Locate and identify every blood parasite.
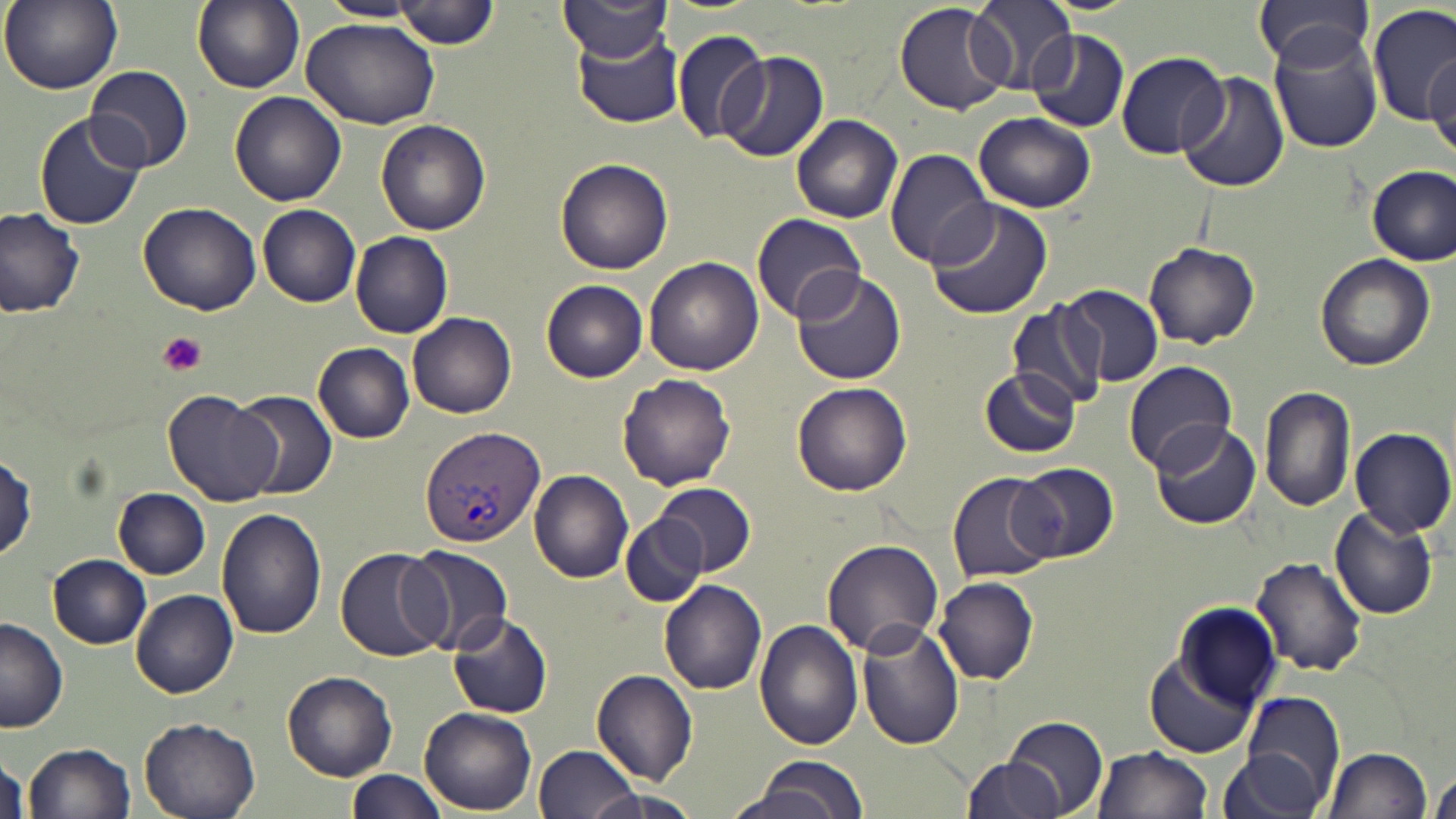
Approximate bounding boxes as [x1, y1, x2, y2] in pixels.
Plasmodium vivax-infected red blood cells: [420, 427, 545, 548].
No Plasmodium falciparum, Plasmodium ovale, Plasmodium malariae, Babesia divergens, or Trypanosoma brucei observed.

Platelet locations: [156, 331, 209, 376]. Uninfected red blood cell locations: [1, 0, 123, 94], [192, 0, 304, 92], [318, 0, 425, 23], [397, 0, 499, 49], [970, 0, 1079, 92], [1254, 0, 1375, 72], [555, 1, 672, 64], [895, 2, 1012, 115], [1369, 5, 1455, 127], [299, 13, 441, 131], [670, 28, 771, 144], [1028, 28, 1129, 133], [572, 29, 685, 128], [1269, 33, 1383, 154], [1029, 37, 1227, 140], [718, 51, 828, 163], [1116, 51, 1230, 160], [1426, 54, 1456, 158], [86, 65, 193, 175], [1175, 70, 1291, 192], [229, 92, 346, 207], [971, 109, 1096, 214], [34, 112, 146, 231], [791, 113, 902, 223], [375, 120, 491, 236], [885, 149, 995, 267], [555, 157, 673, 276], [1368, 166, 1454, 265], [925, 199, 1054, 320], [138, 201, 262, 315], [257, 205, 361, 307], [0, 207, 84, 317], [751, 213, 866, 322], [351, 232, 453, 338], [1142, 242, 1260, 348], [1315, 254, 1434, 370], [643, 256, 762, 375], [789, 269, 906, 385], [540, 280, 648, 382], [1060, 286, 1163, 386], [1008, 301, 1108, 409], [408, 312, 517, 418], [314, 342, 414, 444], [1122, 361, 1238, 476], [978, 367, 1081, 457], [617, 374, 737, 489], [792, 382, 911, 497], [1259, 385, 1357, 514], [233, 388, 337, 500], [161, 389, 282, 506], [1149, 420, 1263, 531], [1350, 427, 1455, 540], [1, 450, 37, 561], [1012, 462, 1119, 563], [529, 469, 634, 582], [948, 470, 1064, 584], [651, 481, 755, 575], [113, 487, 210, 578], [1328, 507, 1440, 620], [216, 509, 327, 640], [621, 514, 705, 606], [822, 539, 944, 655], [400, 543, 514, 654], [335, 545, 449, 662], [48, 554, 152, 648], [1250, 555, 1368, 679], [935, 576, 1040, 686], [659, 580, 769, 694], [132, 589, 240, 696], [1174, 603, 1280, 706], [448, 611, 553, 719], [0, 617, 68, 733], [753, 621, 863, 753], [857, 623, 965, 749], [1143, 649, 1261, 758], [592, 669, 699, 784], [282, 670, 397, 780], [1241, 692, 1345, 806], [420, 708, 536, 815], [138, 715, 263, 819], [1004, 715, 1109, 819], [23, 741, 136, 819], [532, 742, 642, 819], [1092, 744, 1214, 819], [1321, 745, 1433, 819], [0, 749, 30, 819], [1218, 750, 1324, 819], [739, 756, 870, 819], [961, 757, 1066, 819], [1431, 762, 1456, 819], [346, 768, 448, 819], [574, 786, 700, 819]. Slide-level diagnosis: Plasmodium vivax. Thin blood smear. Image is 1456×819 pixels. May-Grünwald-Giemsa stain. Optical microscopy. Single field of view. 1000x magnification.